Classify this cell by malaria status.
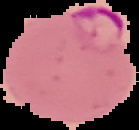

It is parasitized.

Summary:
  - Preparation: thin blood film
  - Image size: 139×130 pixels
  - Image type: cell region segmented out of the field of view; surrounding area masked to black